Assess the morphology of the red blood cells.
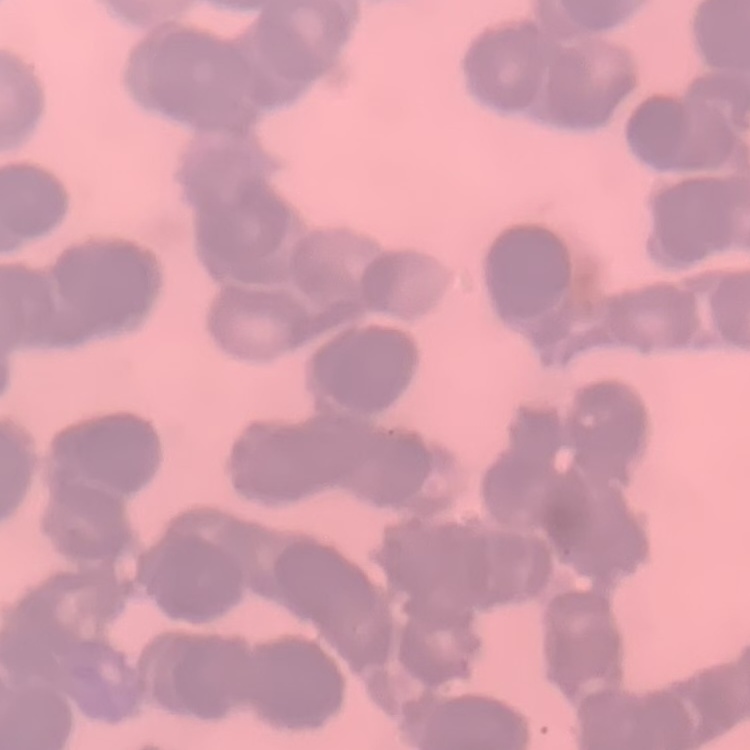

Rouleaux formation.

image type = square crop of a larger photomicrograph
stain = Field's or Giemsa
preparation = thin peripheral smear